Assess this cell for malaria.
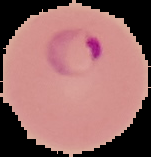

Parasitized.

preparation = thin blood smear
image size = 151×157 pixels
image type = segmented cell region with the area outside set to black